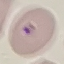
Summary:
  - Malaria status: parasitized
  - Image type: cell patch, automatically extracted from a larger field of view and resized to 64 × 64 pixels
  - Stain: Giemsa
  - Preparation: thin blood smear
  - Capture: smartphone camera at the microscope eyepiece